Name the blood parasite species.
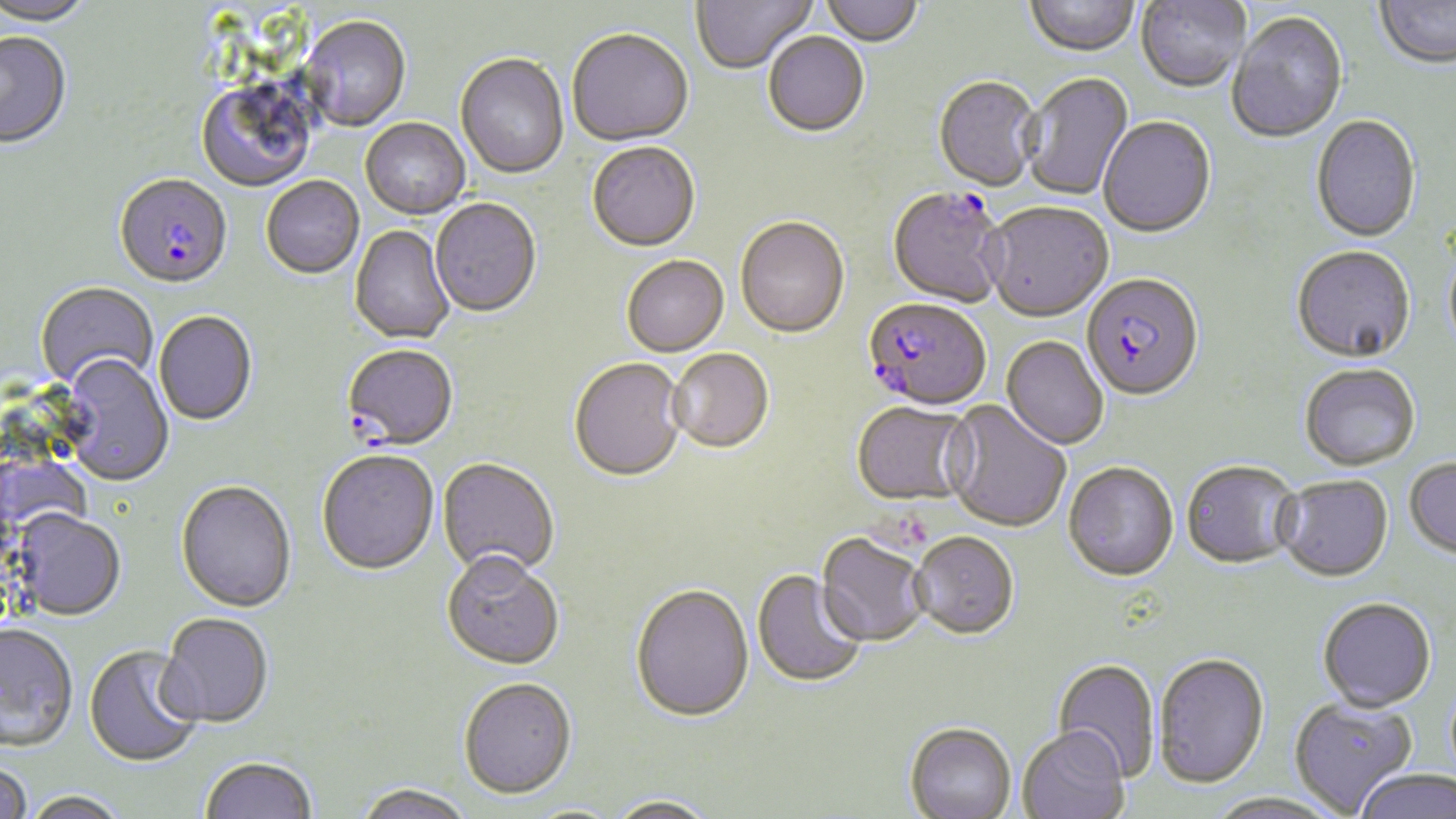
Plasmodium falciparum.

modality: light microscopy
stain: May-Grünwald-Giemsa
image_size: 1456×819 pixels
preparation: thin blood film
field_of_view: one of a larger specimen
magnification: 1000x
plasmodium_falciparum_infected_red_blood_cell_locations: 'approximate bounding boxes as named x1/y1/x2/y2 corners in pixels: (x1=113, y1=176, x2=233, y2=292), (x1=887, y1=189, x2=1008, y2=310), (x1=1081, y1=276, x2=1204, y2=404), (x1=863, y1=300, x2=990, y2=413), (x1=341, y1=345, x2=459, y2=452)'
uninfected_red_blood_cell_locations: 'approximate bounding boxes as named x1/y1/x2/y2 corners in pixels: (x1=0, y1=0, x2=94, y2=28), (x1=692, y1=0, x2=817, y2=76), (x1=820, y1=0, x2=923, y2=49), (x1=1025, y1=0, x2=1140, y2=59), (x1=1136, y1=0, x2=1250, y2=95), (x1=1375, y1=0, x2=1456, y2=72), (x1=1226, y1=13, x2=1348, y2=146), (x1=302, y1=17, x2=411, y2=132), (x1=567, y1=31, x2=694, y2=149), (x1=0, y1=33, x2=72, y2=151), (x1=763, y1=34, x2=869, y2=139), (x1=455, y1=54, x2=569, y2=180), (x1=1020, y1=73, x2=1134, y2=202), (x1=933, y1=78, x2=1042, y2=194), (x1=195, y1=80, x2=318, y2=193), (x1=1311, y1=116, x2=1421, y2=244), (x1=1099, y1=117, x2=1216, y2=240), (x1=360, y1=119, x2=470, y2=220), (x1=587, y1=144, x2=700, y2=254), (x1=261, y1=177, x2=364, y2=280), (x1=429, y1=199, x2=541, y2=320), (x1=982, y1=204, x2=1115, y2=325), (x1=735, y1=219, x2=849, y2=341), (x1=349, y1=225, x2=455, y2=346), (x1=1443, y1=244, x2=1456, y2=362), (x1=1291, y1=248, x2=1416, y2=366), (x1=622, y1=257, x2=730, y2=359), (x1=35, y1=282, x2=158, y2=392), (x1=154, y1=311, x2=258, y2=427), (x1=1001, y1=338, x2=1108, y2=451), (x1=668, y1=350, x2=774, y2=456), (x1=58, y1=356, x2=174, y2=487), (x1=568, y1=360, x2=687, y2=484), (x1=1299, y1=366, x2=1420, y2=473), (x1=942, y1=401, x2=1071, y2=534), (x1=850, y1=403, x2=975, y2=510), (x1=316, y1=452, x2=439, y2=578), (x1=437, y1=459, x2=559, y2=580), (x1=1404, y1=459, x2=1456, y2=561), (x1=1181, y1=463, x2=1302, y2=572), (x1=1063, y1=464, x2=1179, y2=584), (x1=1274, y1=478, x2=1393, y2=584), (x1=175, y1=482, x2=297, y2=615), (x1=11, y1=510, x2=127, y2=622), (x1=910, y1=534, x2=1019, y2=643), (x1=815, y1=535, x2=930, y2=649), (x1=442, y1=556, x2=565, y2=673), (x1=751, y1=570, x2=868, y2=690), (x1=630, y1=586, x2=754, y2=725), (x1=1317, y1=599, x2=1437, y2=714), (x1=156, y1=615, x2=274, y2=731), (x1=1, y1=624, x2=79, y2=753), (x1=83, y1=646, x2=203, y2=770), (x1=1152, y1=655, x2=1269, y2=791), (x1=1050, y1=660, x2=1160, y2=783), (x1=458, y1=680, x2=577, y2=803), (x1=1288, y1=698, x2=1418, y2=815), (x1=904, y1=725, x2=1017, y2=819), (x1=1018, y1=730, x2=1129, y2=819), (x1=199, y1=759, x2=318, y2=819), (x1=0, y1=762, x2=33, y2=819), (x1=1354, y1=771, x2=1456, y2=819), (x1=353, y1=785, x2=475, y2=819), (x1=23, y1=792, x2=130, y2=819), (x1=1205, y1=794, x2=1344, y2=819), (x1=604, y1=798, x2=720, y2=819)'